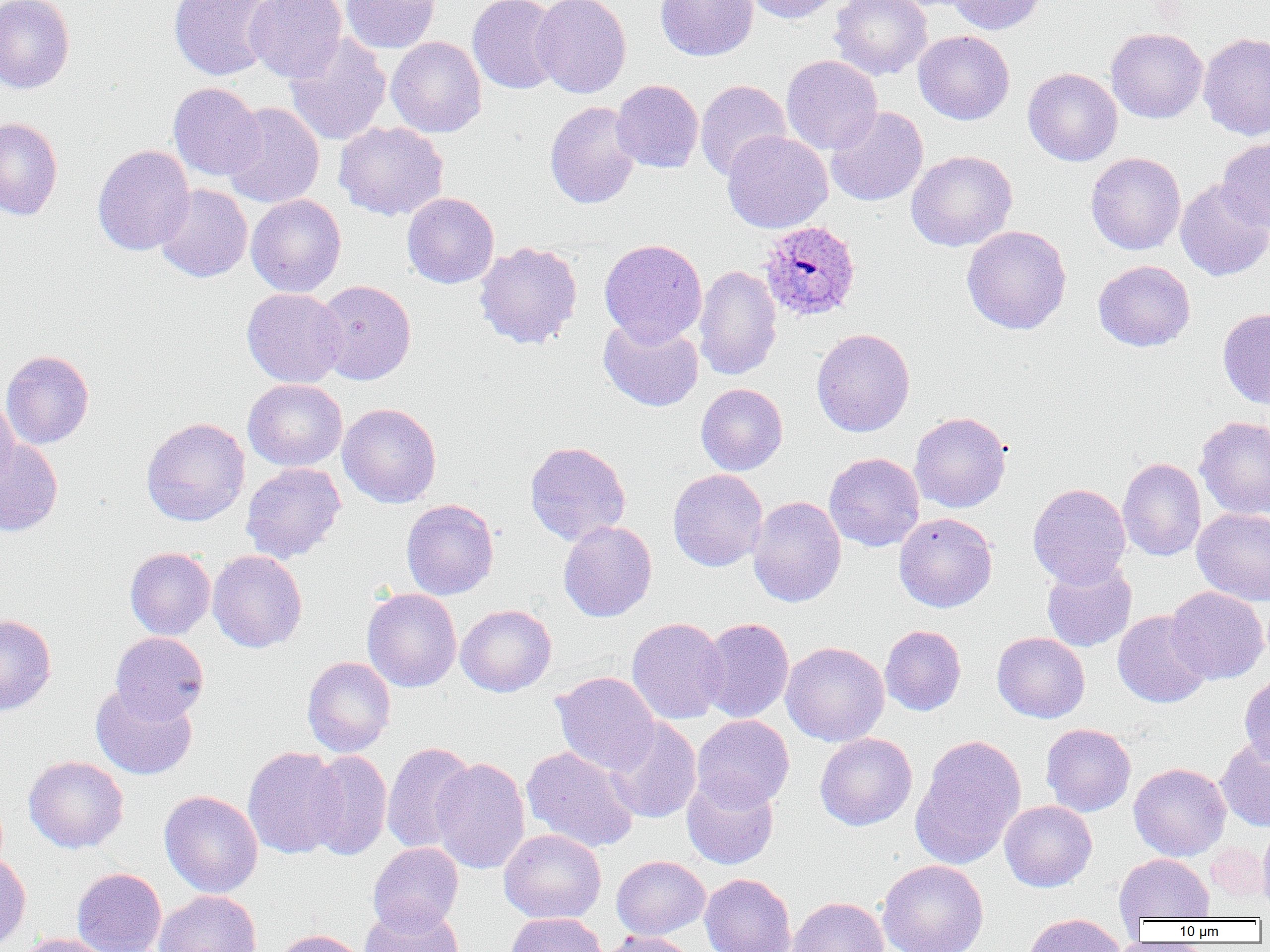

{
  "slide_level_diagnosis": "Plasmodium ovale",
  "modality": "light microscopy",
  "magnification": "1000x",
  "plasmodium_ovale_infected_red_blood_cell_locations": "approximate bounding boxes as [x1, y1, x2, y2] in pixels: [758, 220, 861, 322]",
  "uninfected_red_blood_cell_locations": "approximate bounding boxes as [x1, y1, x2, y2] in pixels: [168, 0, 278, 81], [244, 0, 347, 82], [340, 0, 440, 53], [467, 0, 564, 95], [531, 0, 631, 98], [655, 0, 759, 61], [743, 0, 845, 23], [830, 0, 932, 80], [947, 0, 1046, 35], [0, 1, 75, 93], [1105, 28, 1208, 123], [913, 30, 1014, 124], [1198, 32, 1270, 141], [285, 33, 391, 146], [386, 36, 486, 138], [781, 55, 883, 155], [1023, 68, 1123, 166], [695, 79, 791, 181], [611, 80, 703, 173], [168, 82, 266, 181], [544, 101, 642, 209], [221, 102, 325, 208], [825, 107, 928, 206], [0, 117, 63, 220], [334, 121, 449, 221], [722, 130, 833, 233], [1217, 137, 1270, 232], [92, 144, 195, 256], [906, 150, 1017, 252], [1085, 152, 1186, 255], [1175, 179, 1270, 281], [154, 184, 253, 283], [402, 193, 499, 288], [245, 194, 346, 297], [961, 225, 1072, 335], [599, 238, 707, 346], [474, 241, 583, 349], [1093, 260, 1195, 352], [694, 264, 782, 381], [315, 280, 416, 384], [241, 287, 347, 387], [1218, 307, 1270, 409], [598, 317, 703, 412], [811, 328, 915, 436], [1, 350, 94, 449], [243, 378, 348, 471], [695, 383, 788, 475], [0, 396, 19, 493], [338, 402, 441, 508], [910, 411, 1012, 513], [1195, 415, 1270, 520], [141, 417, 250, 526], [0, 436, 63, 536], [524, 441, 631, 545], [824, 452, 925, 552], [1118, 457, 1206, 561], [241, 462, 346, 564], [667, 469, 768, 571], [1028, 483, 1130, 587], [747, 496, 846, 608], [401, 499, 499, 599], [1192, 507, 1270, 605], [894, 512, 998, 613], [558, 520, 657, 622], [124, 547, 215, 640], [207, 550, 307, 653], [1041, 559, 1137, 652], [1166, 586, 1269, 684], [362, 588, 462, 692], [456, 604, 556, 696], [1112, 610, 1212, 708], [0, 614, 57, 716], [626, 617, 729, 724], [697, 618, 794, 723], [880, 625, 966, 716], [698, 629, 888, 728], [110, 631, 209, 723], [992, 632, 1090, 723], [781, 641, 889, 746], [302, 656, 396, 757], [551, 671, 660, 777], [1240, 671, 1270, 767], [91, 683, 197, 780], [691, 715, 794, 810], [604, 717, 702, 824], [1041, 723, 1136, 817], [814, 732, 918, 831], [910, 734, 1027, 869], [1216, 737, 1270, 832], [381, 741, 477, 854], [242, 746, 346, 859], [521, 746, 640, 853], [304, 750, 392, 860], [23, 755, 129, 853], [430, 757, 531, 874], [1129, 763, 1231, 861], [682, 772, 779, 870], [159, 790, 263, 898], [999, 800, 1097, 892], [1257, 821, 1270, 913], [499, 828, 606, 924], [1205, 840, 1268, 903], [368, 842, 464, 933], [0, 852, 31, 951], [1114, 854, 1214, 922], [611, 855, 710, 939], [877, 859, 988, 952], [72, 867, 167, 952], [699, 873, 796, 952], [154, 890, 262, 952], [788, 896, 888, 952], [360, 904, 464, 952], [506, 913, 607, 952], [1023, 913, 1126, 952], [271, 928, 368, 952], [600, 930, 698, 952], [18, 933, 115, 952]",
  "field_of_view": "one of a larger specimen",
  "preparation": "thin blood film",
  "image_size": "1270×952 pixels"
}